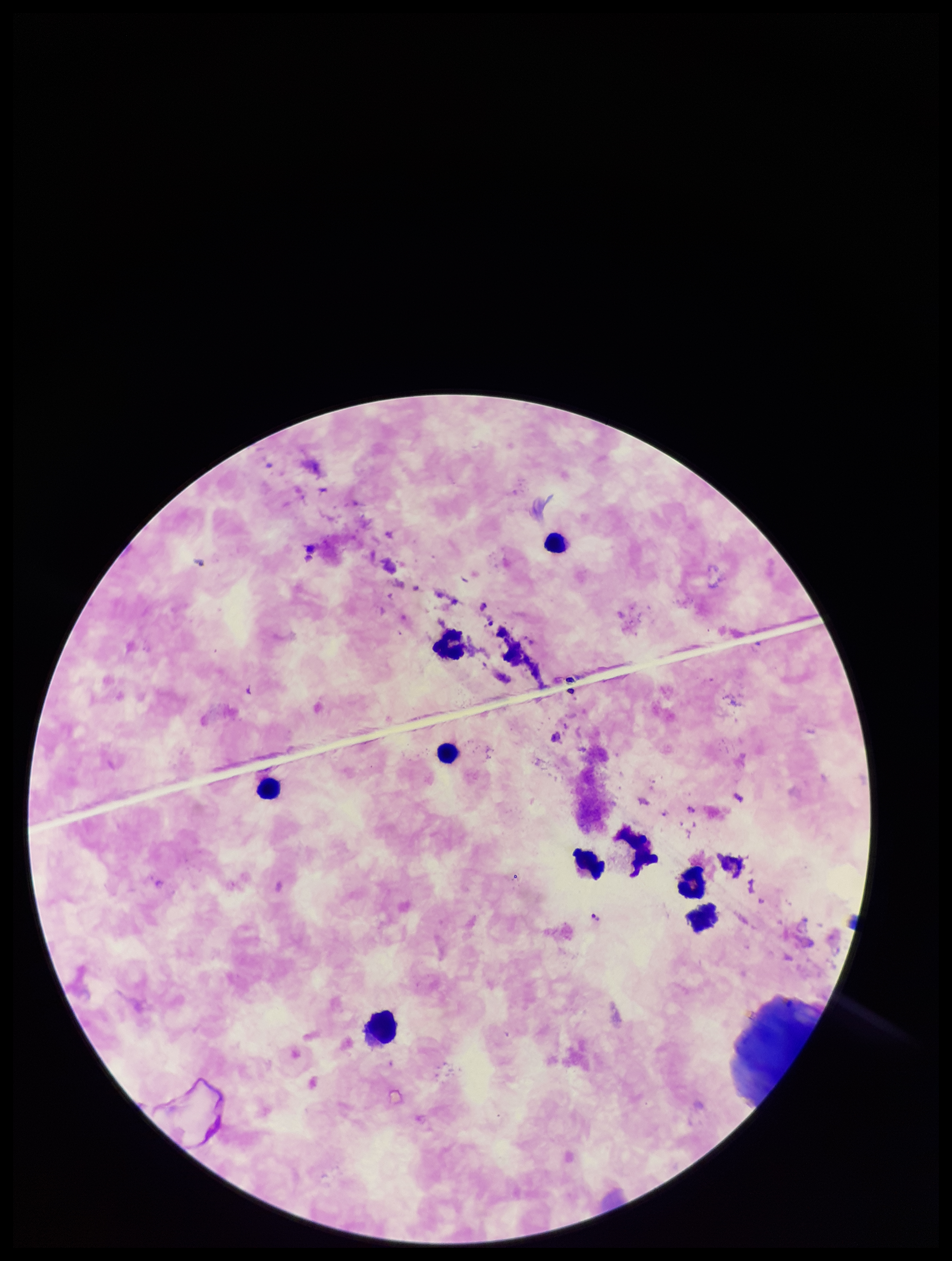

field of view = one from this slide
Plasmodium parasites = detected
species reported for this patient = Plasmodium falciparum
leukocyte count = 9
preparation = thick smear
stain = Giemsa
capture = smartphone photograph through the microscope eyepiece
image size = 952×1261 pixels
patient malaria status = infected
parasite count = 2